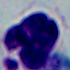 Captured at 1000x magnification. A white blood cell is shown. Photomicrograph.